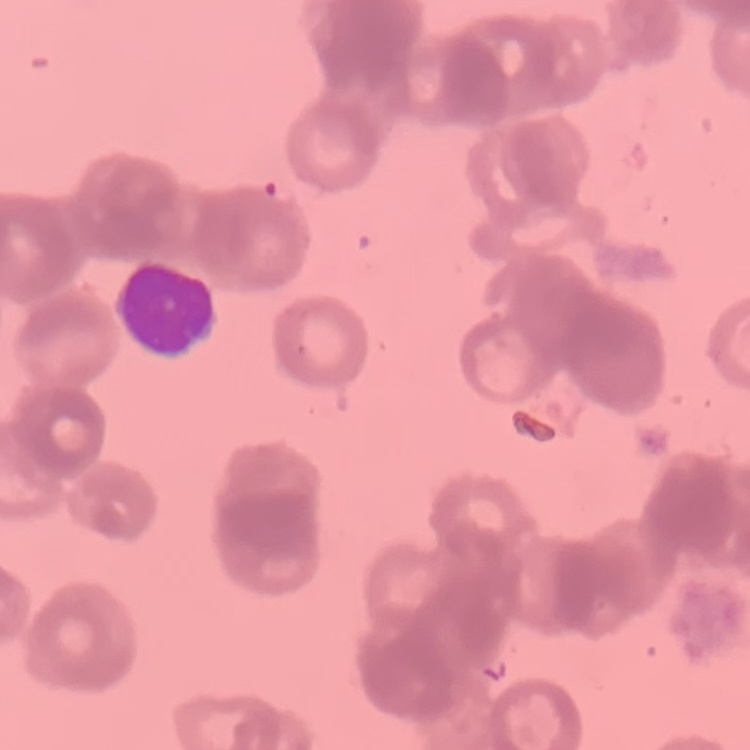

Summary:
  - Red blood cell morphology: rouleaux formation
  - Preparation: thin blood film
  - Image type: square crop of a larger photomicrograph
  - Stain: Field's or Giemsa